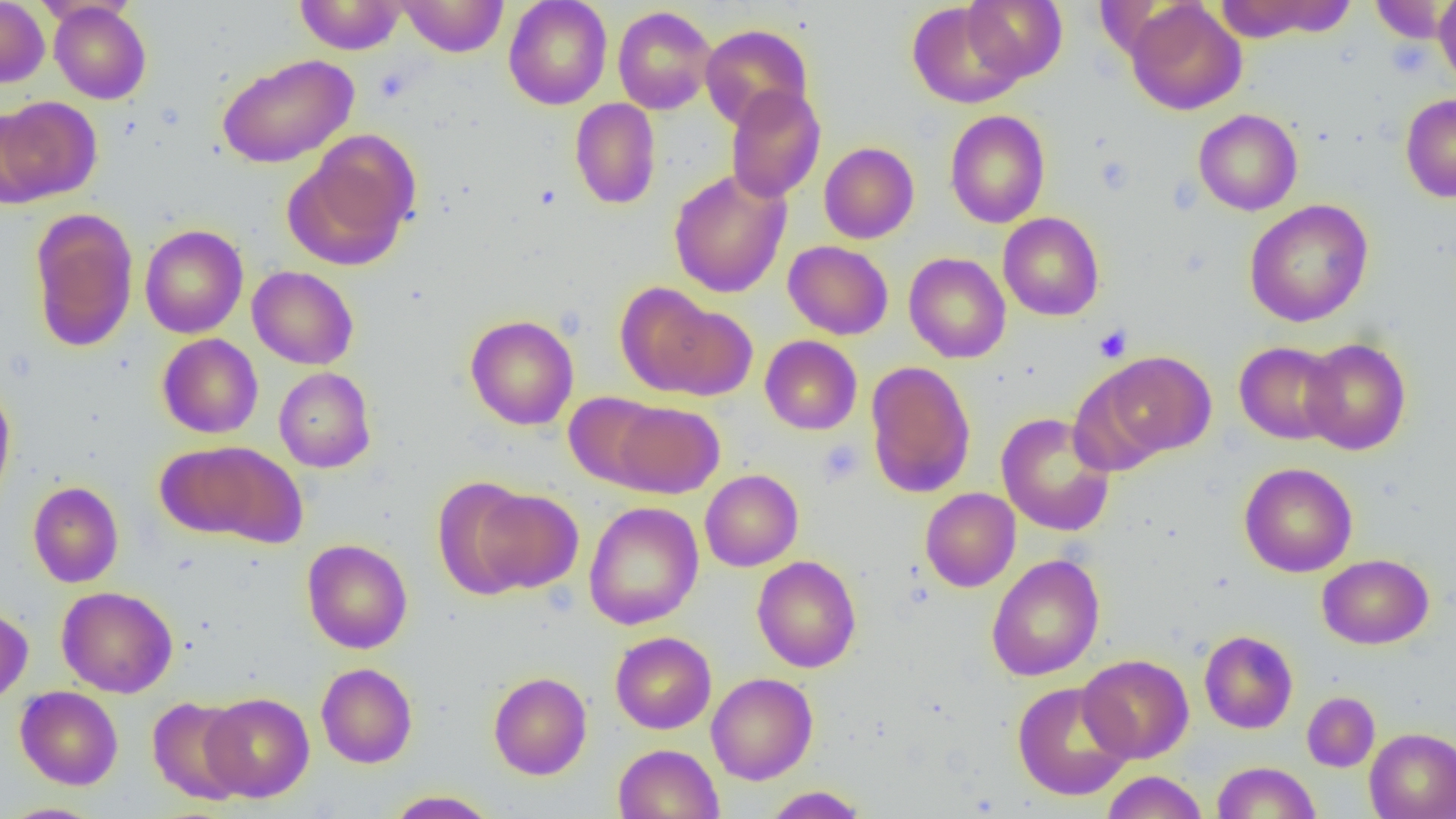

Summary:
  - Coordinate format: approximate bounding boxes as (x1, y1, x2, y2) in pixels
  - Platelet locations: (1389, 39, 1431, 78), (1095, 155, 1136, 195), (1094, 324, 1132, 362), (818, 439, 865, 486)
  - Uninfected red blood cell locations: (0, 0, 50, 87), (294, 0, 406, 55), (397, 0, 509, 57), (503, 0, 612, 110), (962, 0, 1067, 82), (1214, 0, 1357, 42), (1434, 0, 1456, 88), (907, 1, 1025, 108), (1126, 1, 1247, 116), (1371, 1, 1455, 44), (49, 2, 151, 104), (613, 5, 717, 114), (700, 23, 814, 130), (216, 53, 358, 168), (725, 85, 826, 203), (1400, 93, 1456, 203), (0, 96, 102, 204), (569, 98, 661, 210), (1193, 109, 1303, 216), (944, 110, 1050, 228), (284, 135, 419, 272), (819, 142, 919, 244), (668, 169, 791, 298), (1244, 199, 1374, 327), (28, 208, 138, 353), (998, 212, 1104, 321), (140, 224, 248, 338), (783, 240, 893, 339), (903, 253, 1011, 363), (247, 266, 359, 370), (615, 282, 734, 397), (465, 314, 579, 430), (157, 333, 263, 438), (760, 335, 862, 435), (1299, 337, 1412, 455), (1234, 341, 1342, 444), (1096, 351, 1216, 460), (865, 361, 976, 499), (274, 367, 375, 472), (0, 381, 16, 507), (564, 391, 667, 489), (612, 401, 724, 498), (997, 412, 1115, 536), (158, 442, 303, 544), (1238, 462, 1358, 577), (700, 469, 803, 572), (433, 478, 539, 597), (27, 481, 124, 587), (920, 487, 1020, 592), (469, 488, 584, 594), (584, 501, 704, 630), (301, 539, 413, 654), (986, 554, 1105, 681), (1318, 554, 1434, 649), (752, 556, 861, 672), (56, 586, 178, 697), (0, 604, 33, 705), (1199, 630, 1298, 734), (610, 631, 716, 734), (1078, 654, 1193, 763), (316, 662, 418, 768), (488, 671, 592, 780), (706, 672, 818, 784), (1012, 681, 1134, 800), (15, 686, 123, 790), (1302, 691, 1380, 771), (200, 692, 315, 802), (147, 696, 249, 805), (1364, 728, 1456, 819), (613, 743, 723, 819), (1212, 761, 1321, 818), (1101, 771, 1209, 819), (762, 785, 868, 818), (384, 790, 499, 818), (0, 803, 107, 819)
  - Slide-level diagnosis: negative for blood parasites
  - Field of view: single
  - Magnification: 1000x
  - Preparation: thin blood smear
  - Image size: 1456×819 pixels
  - Modality: optical microscopy